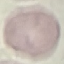
Summary:
  - Result: no malaria parasites detected
  - Preparation: thin blood film
  - Image type: automatically extracted cell patch, resized to 64 × 64 pixels
  - Capture: smartphone camera at the microscope eyepiece
  - Stain: Giemsa